Assess the morphology of the red blood cells.
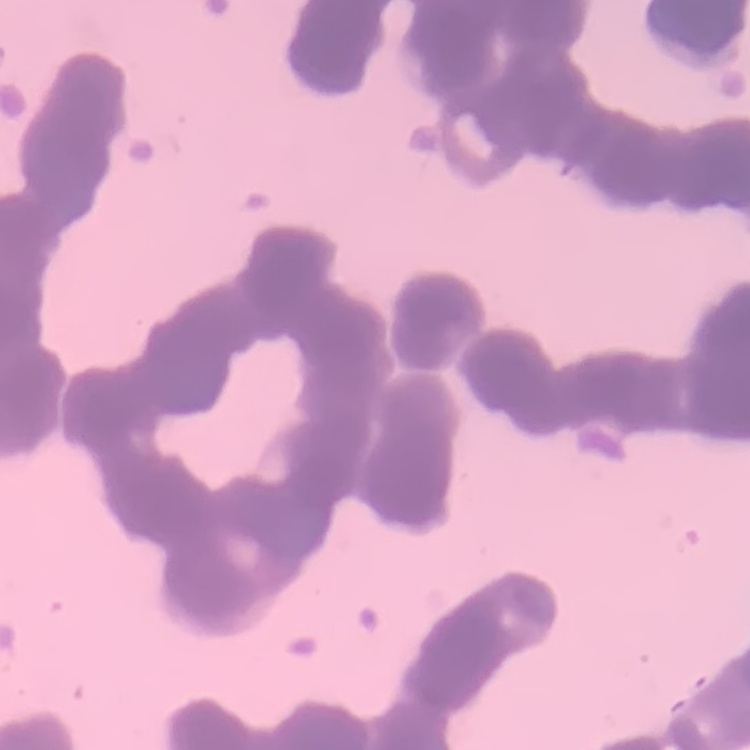

Rouleaux formation.

Square crop of a larger photomicrograph. Thin blood film. Field's or Giemsa stain.